Classify this cell by malaria status.
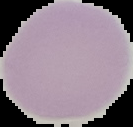

Uninfected.

preparation = thin blood film
image size = 133×127 pixels
image type = cell region segmented out of the field of view; surrounding area masked to black